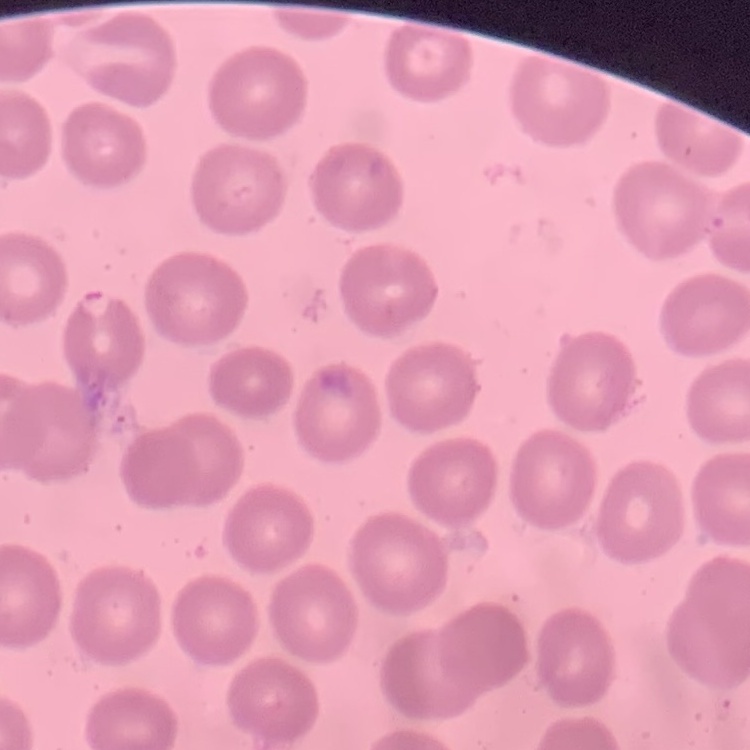 The red blood cells show no rouleaux formation. One tile cut from a larger photomicrograph. Field's or Giemsa stain. Thin blood film.